Identify the blood parasite species.
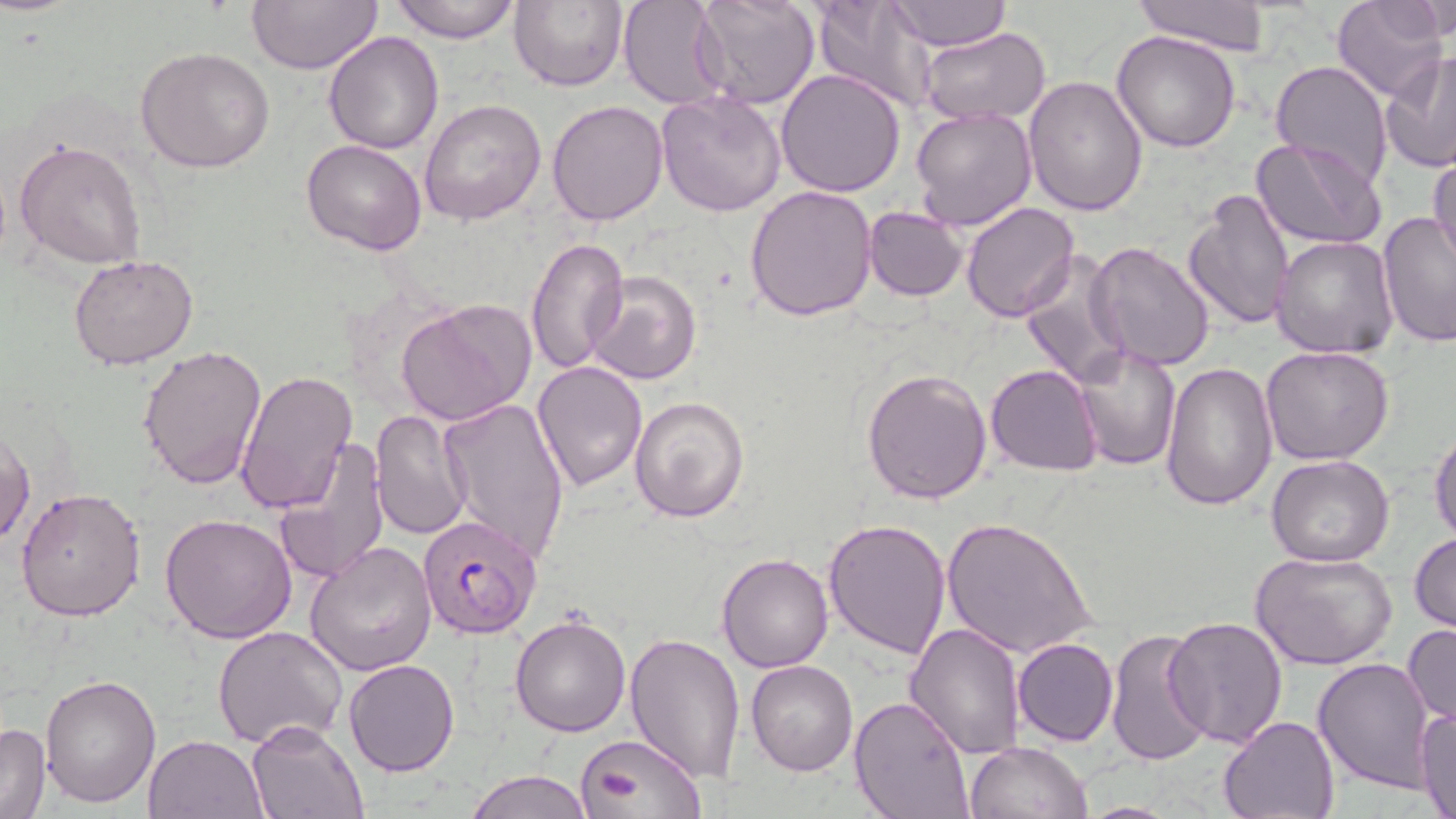

Plasmodium falciparum.

{
  "preparation": "thin blood film",
  "modality": "light microscopy",
  "plasmodium_falciparum_infected_red_blood_cell_locations": "approximate bounding boxes as (x1,y1)-(x2,y2) corner pairs in pixels: (417,515)-(541,639)",
  "stain": "May-Grünwald-Giemsa",
  "uninfected_red_blood_cell_locations": "approximate bounding boxes as (x1,y1)-(x2,y2) corner pairs in pixels: (246,0)-(383,74), (389,0)-(522,43), (508,0)-(629,92), (618,0)-(732,108), (690,0)-(820,110), (811,0)-(937,114), (1130,0)-(1273,55), (1332,0)-(1446,101), (886,1)-(1011,50), (1406,1)-(1453,44), (919,28)-(1052,126), (323,31)-(446,153), (1111,31)-(1241,152), (136,47)-(277,172), (1380,50)-(1456,176), (1270,60)-(1394,186), (775,68)-(907,197), (1022,75)-(1149,217), (655,91)-(785,216), (419,98)-(547,224), (546,100)-(668,226), (910,104)-(1038,231), (1251,136)-(1388,251), (14,138)-(148,269), (302,139)-(428,255), (1429,152)-(1456,271), (745,184)-(879,322), (1184,186)-(1296,329), (959,202)-(1080,323), (862,207)-(967,300), (1377,212)-(1456,348), (526,235)-(628,377), (1272,235)-(1400,358), (1087,242)-(1218,372), (68,254)-(200,370), (1019,254)-(1130,388), (587,271)-(701,385), (396,299)-(538,426), (138,344)-(268,490), (1072,345)-(1181,470), (1260,346)-(1393,466), (1161,360)-(1279,511), (533,361)-(647,491), (987,364)-(1103,477), (862,367)-(993,504), (236,369)-(358,516), (628,394)-(749,523), (437,397)-(570,562), (370,409)-(474,540), (0,428)-(34,551), (1430,428)-(1456,548), (278,434)-(390,583), (1267,455)-(1394,567), (14,487)-(147,620), (160,514)-(298,644), (823,517)-(951,659), (941,518)-(1096,659), (1409,532)-(1456,633), (306,539)-(438,676), (1250,551)-(1397,670), (717,553)-(834,672), (509,612)-(631,737), (1163,615)-(1289,749), (905,622)-(1029,758), (1404,622)-(1455,727), (211,626)-(348,749), (1105,628)-(1213,766), (624,632)-(746,783), (1013,637)-(1118,745), (344,658)-(460,776), (1313,658)-(1435,791), (746,659)-(859,776), (41,674)-(161,808), (849,696)-(974,819), (1415,707)-(1456,819), (1218,715)-(1339,819), (246,719)-(367,817), (0,722)-(50,819), (580,732)-(705,819), (142,733)-(266,818), (964,740)-(1093,819), (467,769)-(593,819)",
  "field_of_view": "single",
  "image_size": "1456×819 pixels",
  "magnification": "1000x"
}